Name the parasite shown.
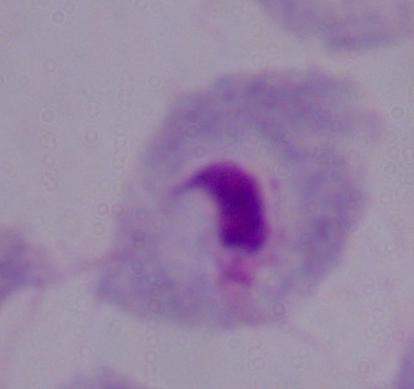

This is a trichomonad.

Captured at 1000x magnification. Micrograph.